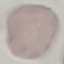
malaria_status: uninfected
preparation: thin smear
capture: smartphone camera at the microscope eyepiece
image_type: automatically extracted cell patch, resized to 64 × 64 pixels
stain: Giemsa